State which parasite is depicted.
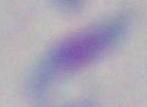

Toxoplasma gondii.

Summary:
  - Modality: micrograph
  - Magnification: 1000x